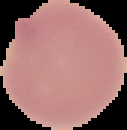 Cell region segmented out of the field of view; the surrounding area is masked to black. Malaria status: uninfected. Image is 127×130 pixels. From a thin blood film.